State which parasite is depicted.
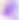
This is Toxoplasma gondii.

{
  "magnification": "400x",
  "modality": "photomicrograph"
}